State which parasite is depicted.
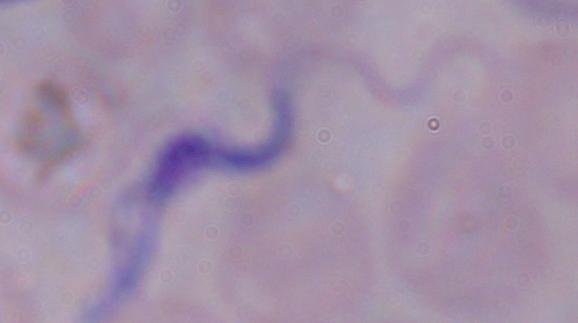
This is a trypanosome.

Summary:
  - Modality: photomicrograph
  - Magnification: 1000x